Classify the preparation.
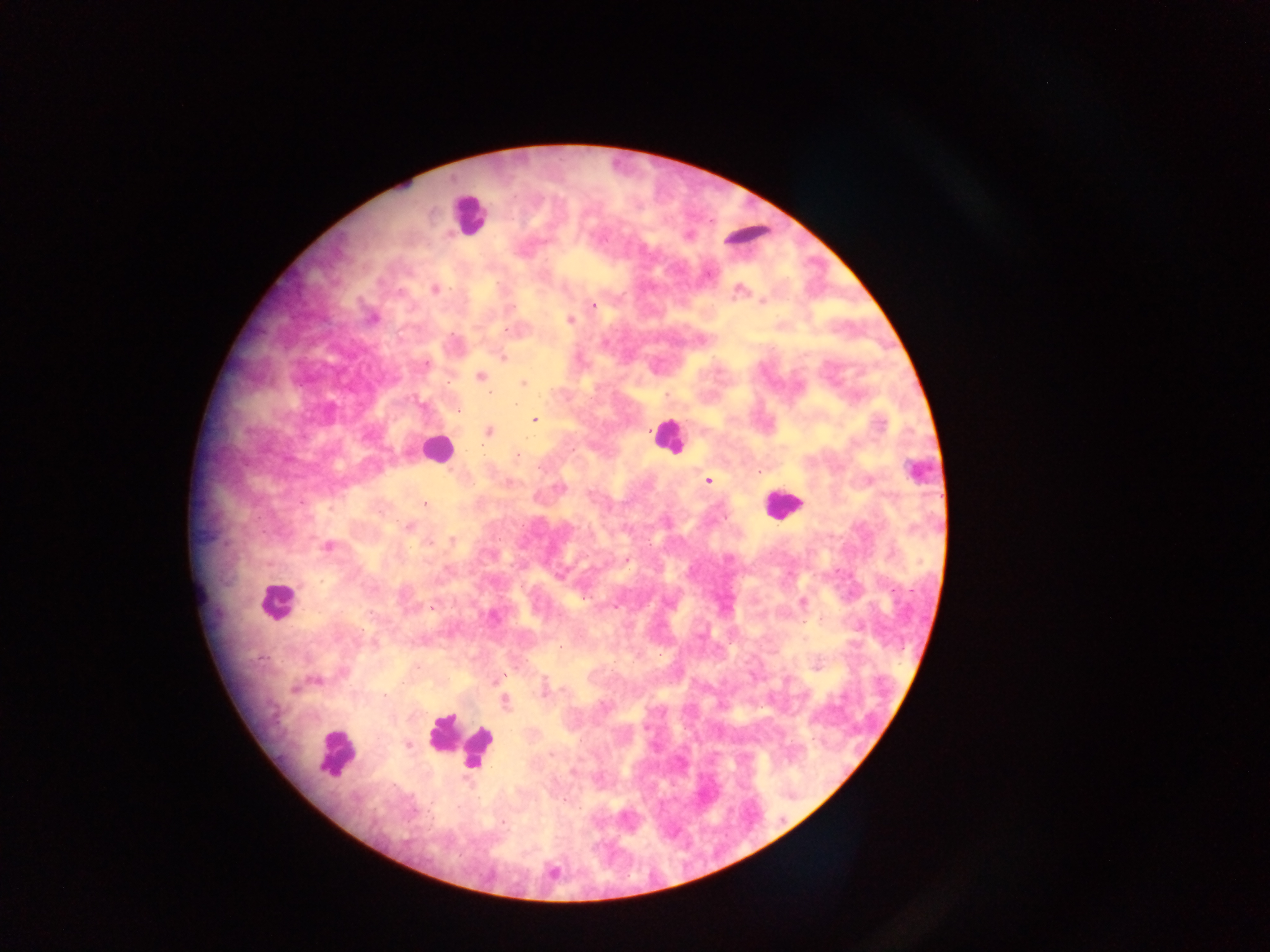

Thick blood film.

capture: mobile-phone photograph through a microscope
object_labeled_both_plasmodium_parasite_and_leukocyte_by_the_source: 'approximate centers as x y in pixels: 918 472'
plasmodium_parasite_locations: 'approximate centers as x y in pixels: 740 289; 434 290; 762 302; 594 306; 511 308; 570 320; 506 331; 503 357; 426 364; 480 376; 524 383; 490 393; 458 410; 534 420; 488 431; 518 455; 708 481; 425 505; 409 526; 452 539; 327 546; 627 560; 803 602; 431 608; 559 648; 499 678; 295 689; 384 696; 505 702; 604 706; 408 745; 552 754; 565 801; 502 822'
field_of_view: single
image_size: 1270×952 pixels
country: Ghana
leukocyte_locations: 'approximate centers as x y in pixels: 469 215; 747 232; 667 435; 434 449; 782 503; 276 601; 458 741; 337 752'